Evaluate for Plasmodium parasites.
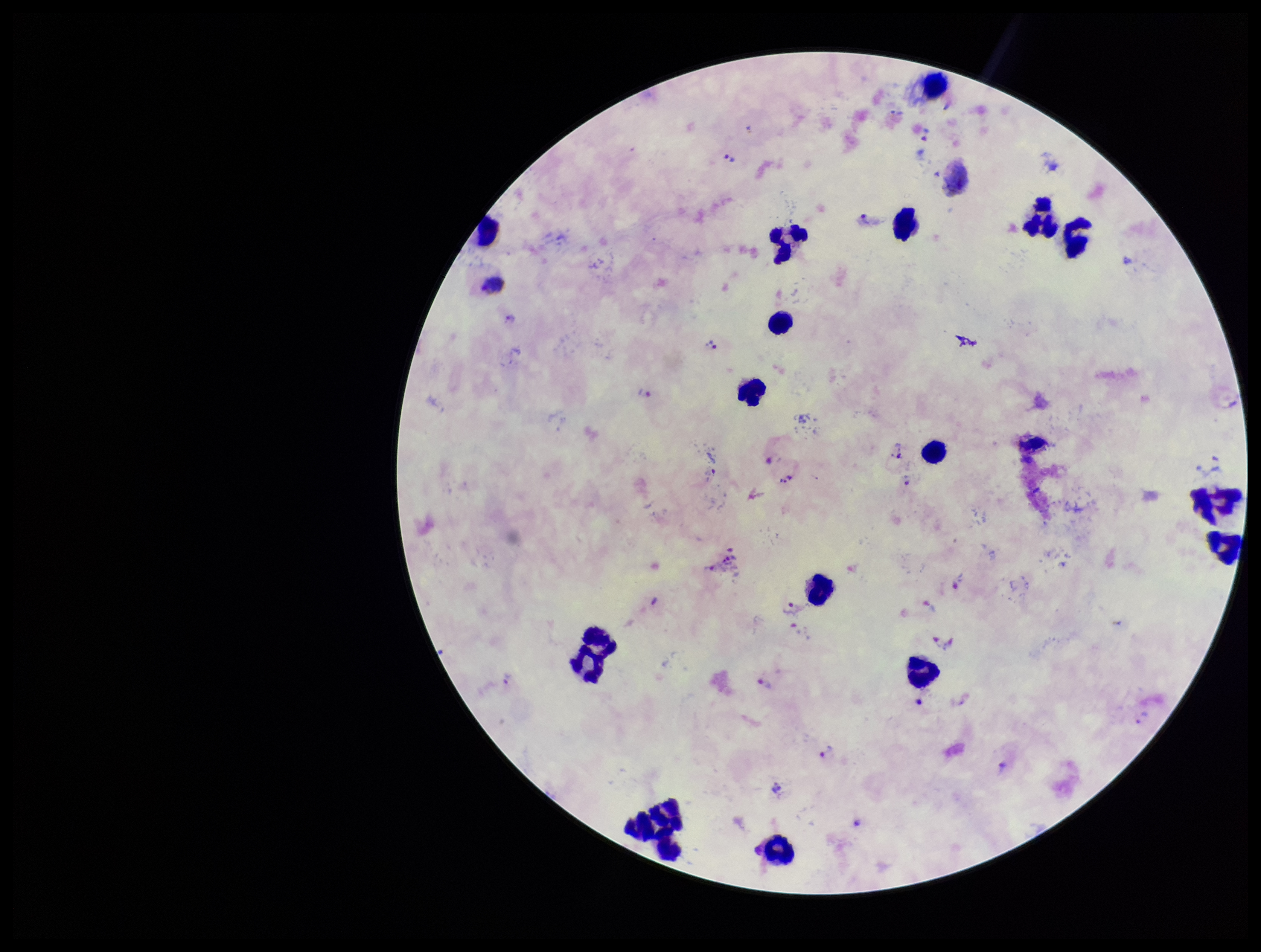

Detected.

capture: smartphone photograph through the microscope eyepiece
leukocyte_count: 18
preparation: thick smear
stain: Giemsa
field_of_view: one from this slide
patient_malaria_status: infected
parasite_count: 23
image_size: 1261×952 pixels
species_reported_for_this_patient: Plasmodium vivax